Describe the morphology of the red blood cells.
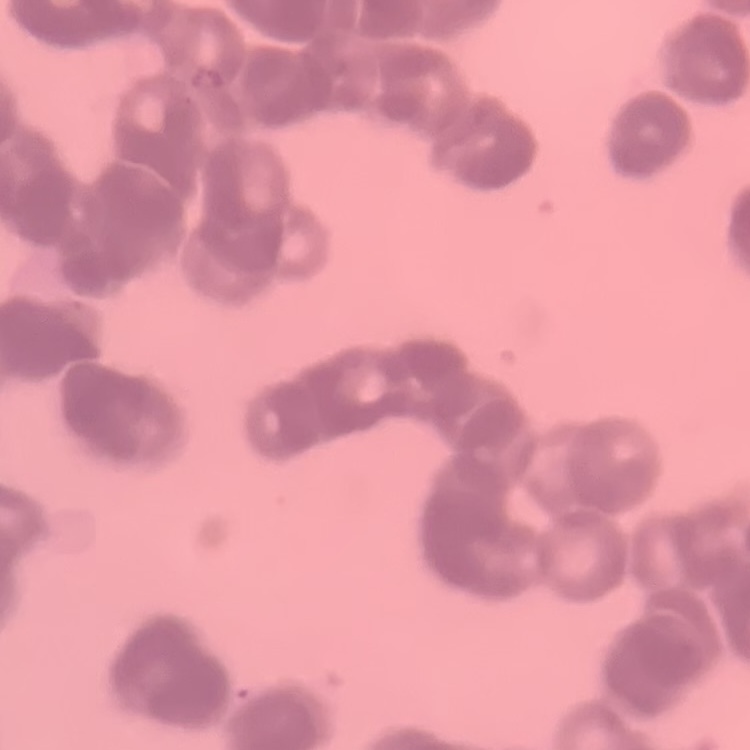
Rouleaux formation.

Field's or Giemsa stain. Thin blood film. One tile cut from a larger photomicrograph.